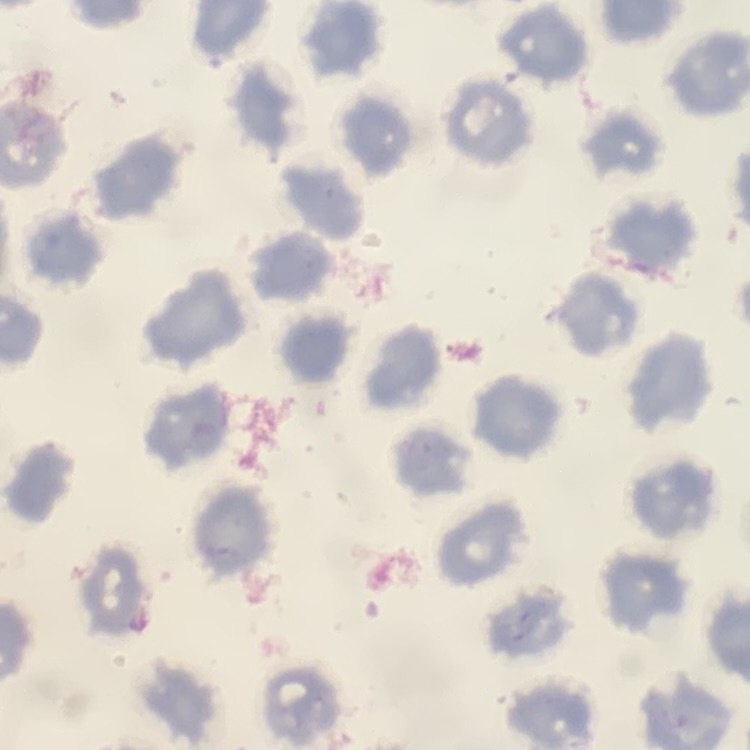

The red blood cells show no rouleaux formation. Field's or Giemsa stain. Thin peripheral smear. Square crop of a larger photomicrograph.